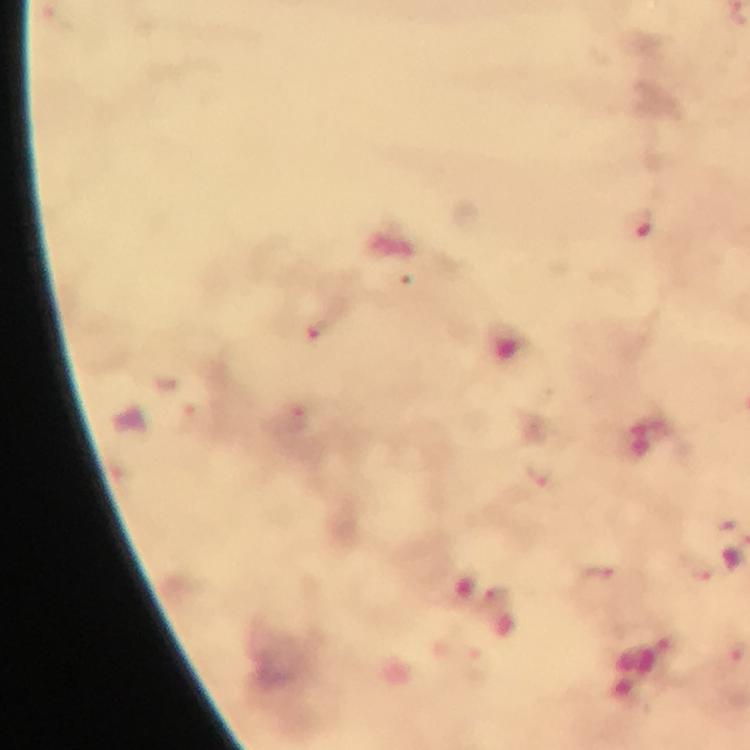
Approximate centers as (x, y) in pixels. Plasmodium parasite locations: (637, 223), (317, 328), (540, 470), (598, 578), (498, 596). Giemsa stain. At 100x magnification. Thick blood film. A crop from one field of view. From a diagnostic examination for malaria. Image is 750×750 pixels. Immersion oil applied. Photographed through the microscope with a smartphone camera.